Locate every Babesia divergens-infected red blood cell.
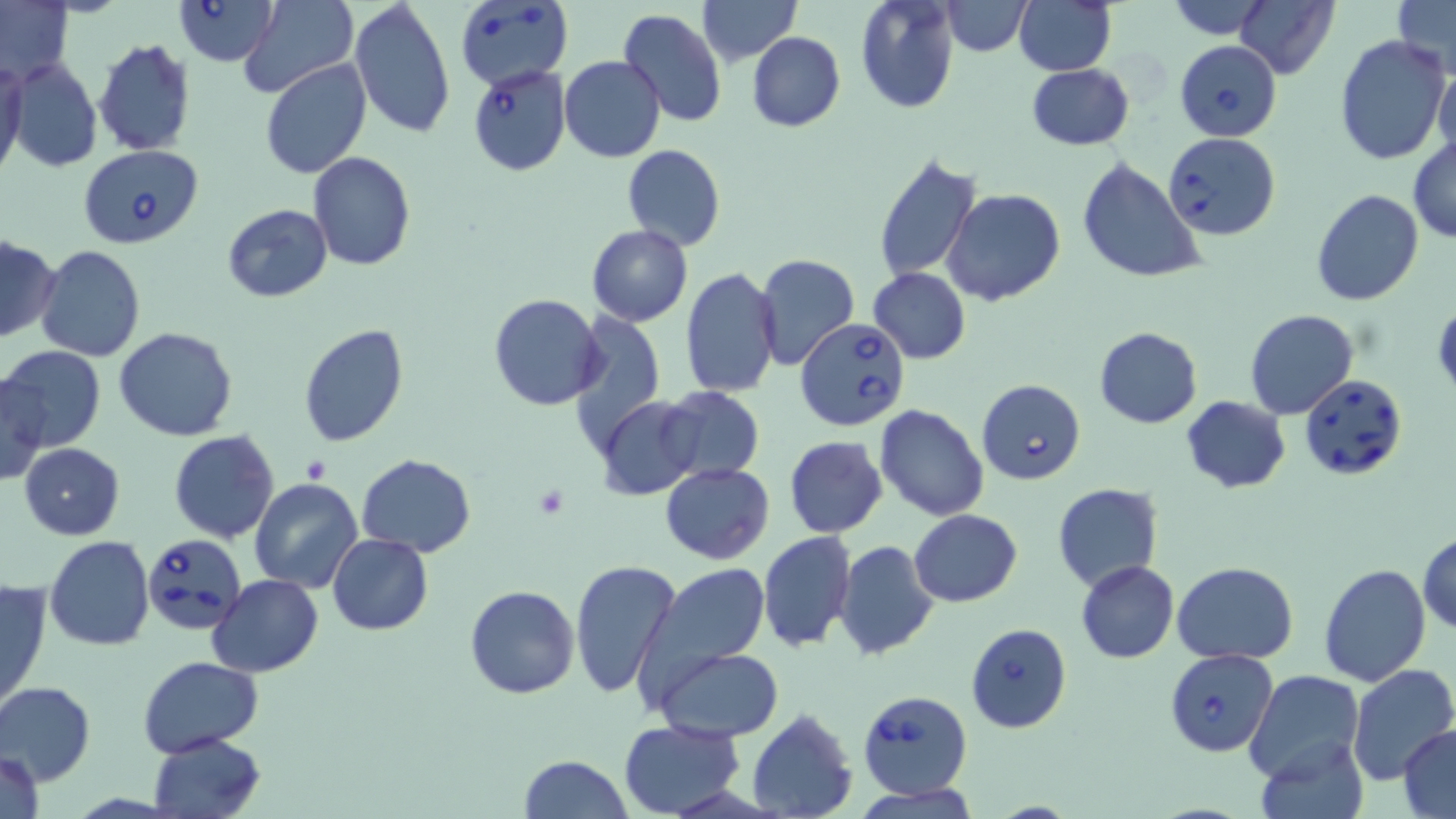

Approximate bounding boxes as [x1, y1, x2, y2] in pixels.
Babesia divergens-infected red blood cells: [173, 0, 279, 65], [455, 2, 572, 90], [1174, 39, 1282, 141], [467, 65, 572, 175], [1164, 132, 1281, 240], [77, 144, 204, 248], [795, 316, 912, 430], [1298, 374, 1409, 481], [978, 381, 1086, 484], [143, 531, 249, 636], [965, 622, 1072, 733], [1165, 648, 1278, 757], [855, 688, 973, 799].

slide-level diagnosis = Babesia divergens
stain = May-Grünwald-Giemsa
field of view = one of a larger specimen
modality = optical microscopy
platelet locations = approximate bounding boxes as [x1, y1, x2, y2] in pixels: [534, 487, 569, 519]
uninfected red blood cell locations = approximate bounding boxes as [x1, y1, x2, y2] in pixels: [239, 0, 356, 99], [350, 0, 456, 142], [699, 0, 801, 65], [854, 0, 960, 114], [1161, 0, 1279, 37], [0, 1, 74, 85], [942, 1, 1031, 56], [1015, 1, 1116, 75], [1233, 1, 1338, 79], [1392, 1, 1455, 78], [616, 8, 726, 128], [747, 32, 845, 132], [1333, 34, 1451, 166], [92, 37, 196, 157], [558, 56, 665, 163], [1432, 57, 1455, 165], [261, 58, 372, 180], [0, 59, 27, 182], [7, 59, 101, 173], [1026, 63, 1135, 150], [1408, 137, 1456, 242], [622, 144, 726, 250], [870, 151, 982, 284], [307, 152, 415, 271], [1076, 157, 1207, 283], [941, 188, 1065, 307], [1310, 189, 1424, 307], [221, 203, 333, 304], [585, 225, 694, 327], [0, 236, 59, 342], [36, 245, 146, 363], [754, 252, 860, 370], [681, 265, 783, 399], [867, 268, 970, 364], [488, 293, 606, 411], [567, 308, 667, 457], [1244, 310, 1358, 420], [298, 323, 407, 448], [115, 326, 238, 442], [1094, 326, 1203, 428], [0, 345, 105, 452], [0, 375, 49, 485], [655, 385, 765, 485], [1181, 395, 1290, 492], [597, 397, 704, 499], [873, 403, 990, 522], [170, 431, 280, 544], [783, 435, 888, 539], [19, 443, 125, 540], [175, 447, 358, 570], [356, 453, 475, 558], [659, 463, 774, 564], [251, 475, 362, 593], [1053, 483, 1163, 592], [909, 509, 1022, 605], [757, 531, 856, 652], [1418, 533, 1456, 633], [327, 534, 433, 634], [45, 537, 155, 653], [835, 541, 939, 660], [570, 558, 682, 700], [1075, 559, 1179, 663], [1172, 561, 1298, 664], [640, 562, 772, 693], [1319, 562, 1431, 686], [207, 574, 325, 676], [0, 577, 51, 712], [465, 585, 579, 698], [651, 646, 782, 741], [140, 655, 263, 757], [1346, 665, 1456, 786], [1244, 670, 1365, 783], [1, 682, 96, 785], [748, 710, 858, 819], [619, 719, 745, 817], [1398, 726, 1456, 816], [147, 732, 264, 819], [1255, 735, 1369, 819], [2, 747, 44, 819], [519, 755, 633, 818], [856, 782, 980, 819]
magnification = 1000x
preparation = thin blood smear
image size = 1456×819 pixels